Give the position of every leukocyte visible.
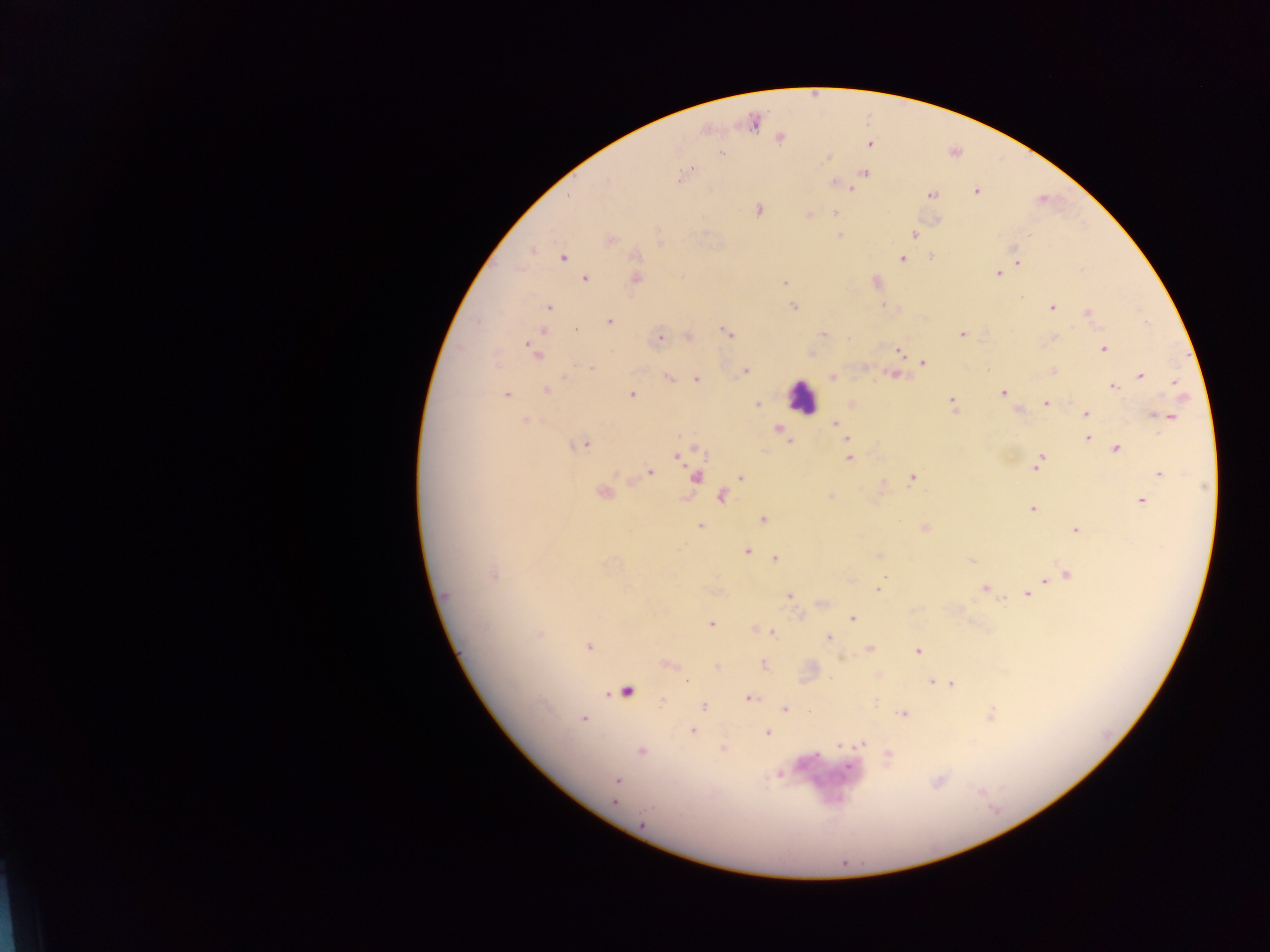
Approximate centers as {x, y} in pixels.
Leukocytes: {801, 397}.

Plasmodium parasite locations: {753, 122}, {779, 138}, {869, 144}, {720, 154}, {863, 173}, {682, 176}, {836, 183}, {851, 187}, {976, 191}, {932, 194}, {758, 210}, {836, 213}, {809, 215}, {839, 234}, {913, 234}, {610, 240}, {532, 250}, {562, 256}, {901, 257}, {931, 257}, {1018, 263}, {997, 273}, {585, 278}, {634, 278}, {785, 282}, {876, 282}, {793, 306}, {885, 306}, {549, 307}, {1052, 307}, {1087, 313}, {609, 322}, {574, 329}, {542, 330}, {726, 332}, {822, 334}, {962, 334}, {688, 336}, {659, 337}, {1103, 348}, {900, 350}, {534, 351}, {812, 353}, {923, 362}, {590, 368}, {745, 371}, {1053, 371}, {895, 374}, {1140, 376}, {831, 377}, {668, 378}, {695, 378}, {1175, 383}, {1112, 387}, {546, 390}, {505, 393}, {1002, 393}, {631, 394}, {1046, 403}, {756, 404}, {852, 404}, {953, 404}, {1017, 409}, {1085, 414}, {1157, 416}, {1168, 417}, {525, 420}, {835, 423}, {779, 429}, {1086, 438}, {847, 439}, {581, 444}, {1115, 448}, {849, 449}, {679, 453}, {849, 458}, {1039, 461}, {650, 472}, {1159, 473}, {741, 476}, {694, 477}, {912, 478}, {603, 492}, {721, 495}, {830, 496}, {1141, 501}, {1032, 508}, {762, 519}, {700, 525}, {924, 528}, {1075, 530}, {746, 550}, {878, 555}, {775, 559}, {971, 560}, {493, 574}, {1067, 574}, {1059, 576}, {1044, 580}, {878, 589}, {985, 589}, {1026, 593}, {445, 596}, {788, 596}, {822, 602}, {852, 617}, {710, 624}, {755, 630}, {772, 631}, {828, 637}, {588, 646}, {869, 649}, {917, 651}, {666, 664}, {763, 664}, {717, 667}, {877, 676}, {685, 680}, {930, 681}, {940, 681}, {951, 683}, {626, 692}, {748, 698}, {703, 706}, {783, 709}, {903, 714}, {989, 716}, {582, 718}, {692, 731}, {767, 733}, {861, 742}, {839, 746}, {723, 748}, {641, 750}, {887, 756}, {779, 773}, {617, 781}, {615, 803}, {642, 825}. Thick blood smear. Image is 1270×952 pixels. One field of view. Sample from Ghana. Photographed through a microscope with a mobile-phone camera.